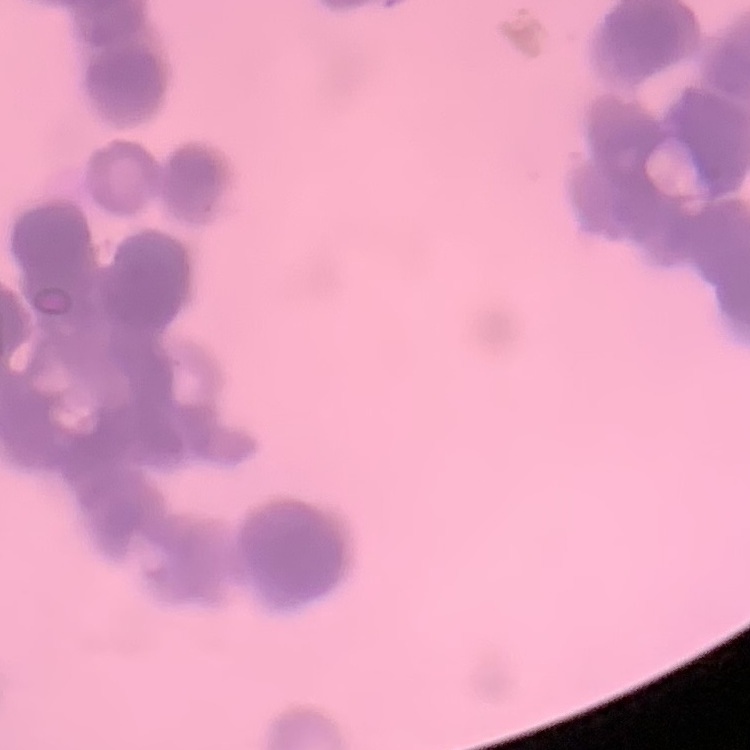
{
  "erythrocyte_morphology": "rouleaux formation",
  "preparation": "thin blood film",
  "stain": "Field's or Giemsa",
  "image_type": "square crop of a larger photomicrograph"
}